State which parasite is depicted.
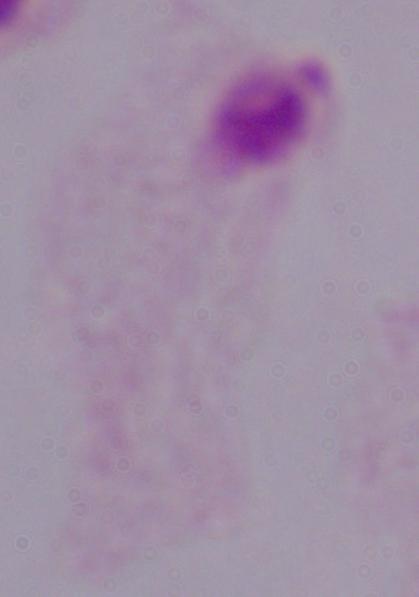

This is a trichomonad.

Summary:
  - Magnification: 1000x
  - Modality: photomicrograph